Identify the blood parasite species.
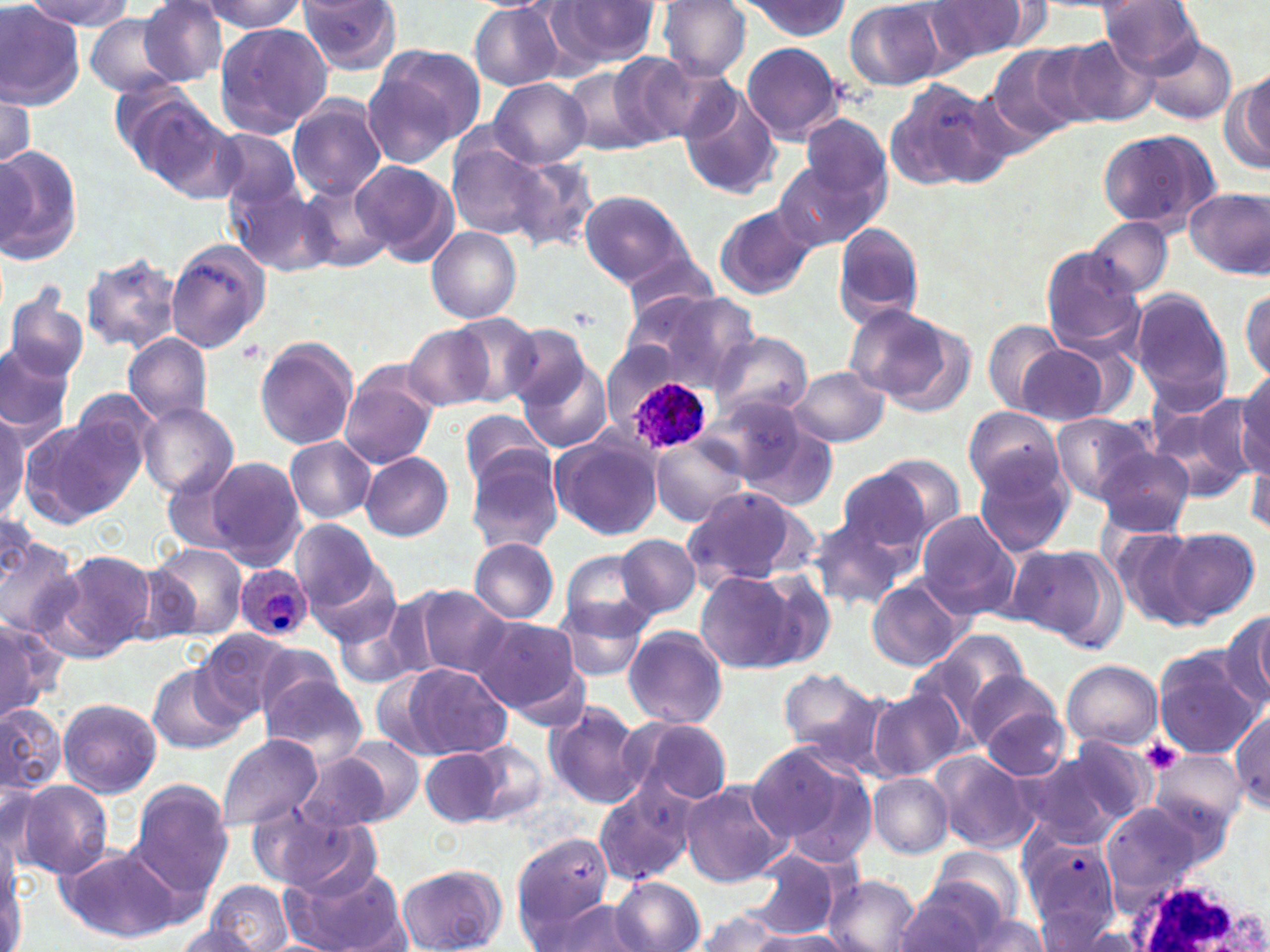
Plasmodium ovale.

white blood cell locations = approximate bounding boxes as [x1, y1, x2, y2] in pixels: [1122, 875, 1265, 952]
platelet locations = approximate bounding boxes as [x1, y1, x2, y2] in pixels: [1142, 738, 1184, 772]
preparation = thin blood film
uninfected red blood cell locations = approximate bounding boxes as [x1, y1, x2, y2] in pixels: [22, 0, 133, 30], [297, 0, 403, 76], [548, 0, 660, 69], [657, 0, 751, 80], [739, 0, 851, 39], [843, 0, 952, 90], [1097, 0, 1207, 78], [0, 1, 84, 109], [200, 1, 307, 33], [925, 2, 1029, 62], [138, 3, 229, 85], [470, 5, 566, 90], [84, 13, 183, 96], [213, 23, 332, 140], [1062, 36, 1156, 127], [1145, 37, 1236, 124], [740, 41, 844, 145], [985, 47, 1092, 145], [364, 48, 482, 164], [608, 53, 698, 145], [1224, 64, 1269, 175], [565, 66, 661, 157], [488, 77, 591, 167], [884, 78, 1007, 192], [110, 81, 215, 178], [677, 84, 783, 201], [1, 90, 35, 178], [286, 96, 387, 200], [136, 106, 242, 203], [800, 113, 889, 206], [208, 127, 304, 211], [1095, 128, 1220, 233], [449, 140, 550, 240], [0, 143, 83, 265], [502, 153, 601, 253], [349, 160, 458, 266], [772, 160, 877, 254], [292, 177, 392, 275], [227, 182, 334, 277], [1187, 186, 1270, 279], [580, 190, 691, 287], [712, 205, 818, 301], [1083, 218, 1174, 297], [831, 221, 923, 327], [427, 228, 519, 324], [165, 239, 267, 352], [1040, 248, 1148, 356], [81, 251, 184, 354], [618, 251, 722, 322], [3, 281, 90, 384], [619, 285, 760, 399], [1240, 285, 1270, 385], [1128, 288, 1233, 411], [844, 304, 971, 414], [439, 313, 544, 407], [982, 318, 1069, 414], [501, 323, 592, 414], [406, 326, 495, 412], [710, 331, 812, 421], [123, 333, 213, 425], [255, 337, 357, 450], [0, 340, 75, 436], [1014, 344, 1116, 424], [517, 358, 612, 453], [788, 367, 892, 447], [338, 368, 437, 469], [1234, 372, 1270, 474], [62, 387, 161, 495], [716, 393, 837, 509], [1145, 393, 1257, 501], [136, 402, 240, 498], [963, 408, 1067, 498], [459, 409, 556, 495], [1049, 412, 1155, 504], [0, 414, 30, 519], [19, 417, 140, 526], [551, 433, 664, 542], [647, 436, 752, 527], [285, 437, 376, 523], [1247, 437, 1270, 540], [1096, 447, 1195, 537], [465, 448, 565, 556], [361, 452, 453, 541], [865, 453, 968, 541], [207, 456, 307, 569], [972, 456, 1074, 557], [160, 464, 249, 559], [831, 470, 933, 568], [680, 487, 815, 588], [914, 510, 1022, 617], [810, 515, 910, 610], [289, 518, 384, 614], [1109, 526, 1210, 631], [1162, 526, 1260, 625], [617, 534, 700, 618], [0, 537, 81, 638], [469, 538, 560, 623], [1010, 540, 1121, 645], [152, 544, 247, 641], [56, 549, 159, 656], [562, 550, 659, 636], [306, 553, 404, 650], [751, 569, 837, 672], [695, 570, 807, 673], [868, 581, 964, 670], [413, 586, 514, 678], [331, 595, 437, 691], [552, 600, 651, 682], [1216, 609, 1269, 710], [1243, 609, 1268, 703], [473, 617, 581, 714], [0, 619, 53, 722], [622, 625, 728, 727], [192, 630, 300, 724], [918, 632, 1026, 726], [1153, 651, 1262, 756], [1060, 659, 1162, 750], [399, 662, 512, 759], [148, 663, 243, 753], [777, 667, 884, 761], [961, 667, 1063, 750], [260, 670, 368, 762], [866, 689, 962, 781], [58, 697, 161, 797], [542, 700, 645, 807], [0, 701, 64, 796], [978, 703, 1071, 781], [1230, 710, 1269, 812], [622, 715, 733, 807], [214, 734, 322, 831], [335, 734, 425, 824], [456, 736, 548, 821], [1020, 742, 1153, 841], [747, 743, 875, 865], [421, 745, 506, 827], [1152, 749, 1247, 830], [930, 752, 1038, 854], [295, 754, 390, 834], [868, 773, 952, 857], [13, 780, 113, 879], [128, 781, 234, 905], [679, 781, 791, 886], [593, 784, 699, 886], [250, 802, 373, 894], [1098, 802, 1218, 898], [510, 834, 616, 942], [1026, 840, 1120, 944], [55, 843, 186, 944], [930, 847, 1026, 926], [0, 850, 26, 949], [743, 852, 838, 937], [395, 864, 504, 952], [282, 865, 410, 952], [823, 874, 920, 952], [612, 877, 704, 951], [895, 879, 1000, 952], [206, 881, 294, 951], [547, 900, 652, 949], [693, 911, 787, 951], [961, 912, 1050, 952], [168, 923, 263, 952], [749, 929, 851, 952]
modality = optical microscopy
image size = 1270×952 pixels
Plasmodium ovale-infected red blood cell locations = approximate bounding boxes as [x1, y1, x2, y2] in pixels: [630, 378, 708, 452], [233, 567, 312, 641]
stain = May-Grünwald-Giemsa
magnification = 1000x
field of view = one of a larger specimen